Identify the preparation type.
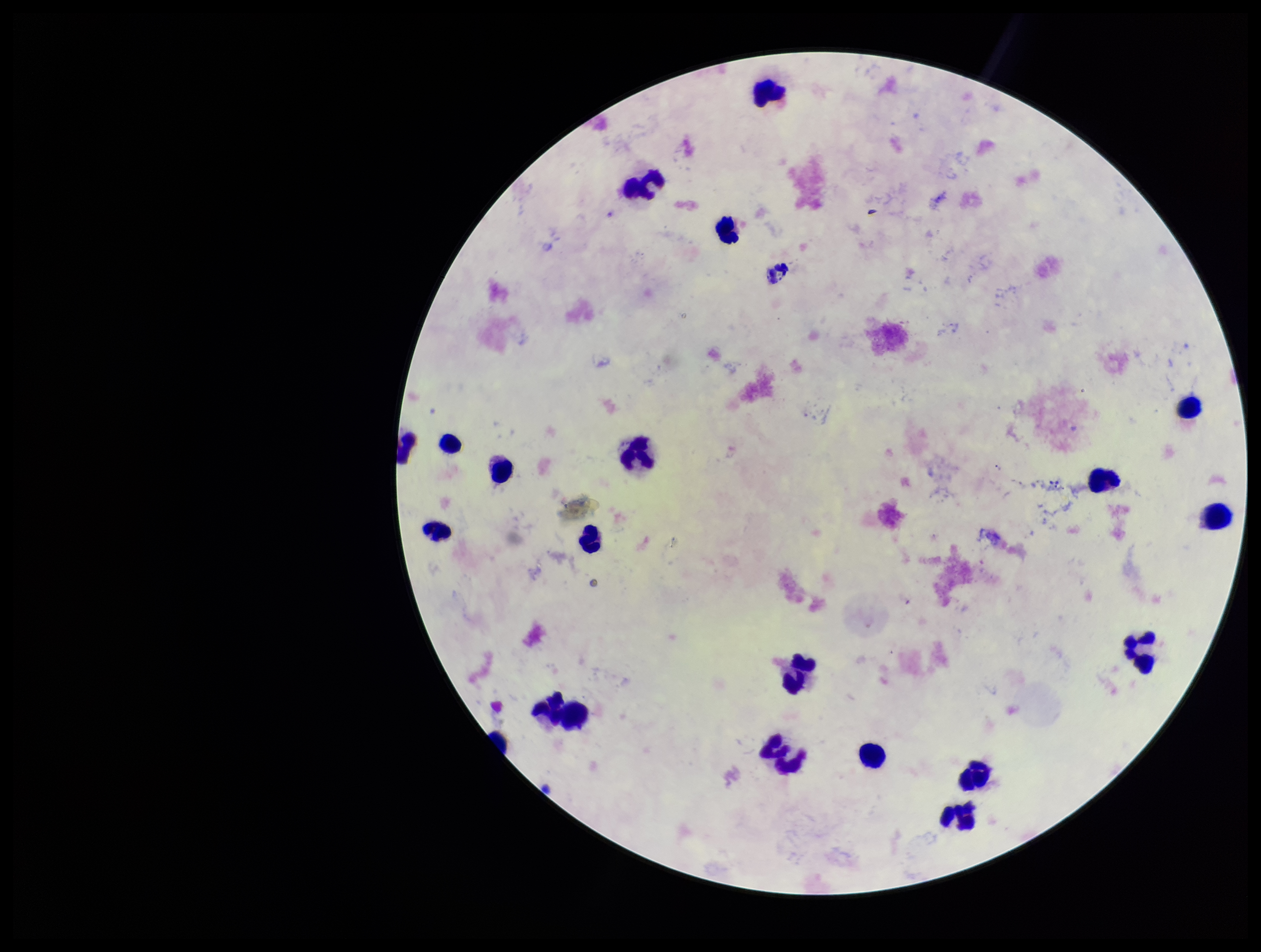

Thick.

Image is 1261×952 pixels. Plasmodium parasites: none seen. Patient malaria status: infected. Species reported for this patient: Plasmodium vivax. Smartphone photograph taken through the eyepiece of a microscope. Leukocyte count: 18. One field from this slide. Stained with Giemsa. Parasite count: 0.